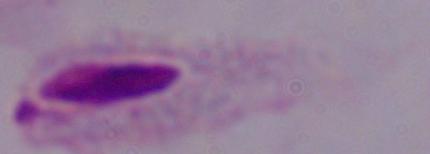
Summary:
  - Modality: micrograph
  - Magnification: 1000x
  - Identification: trichomonad